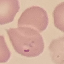
malaria status = parasitized
stain = Giemsa
capture = smartphone through the microscope eyepiece
image type = cell patch, automatically extracted from a larger field of view and resized to 64 × 64 pixels
preparation = thin smear